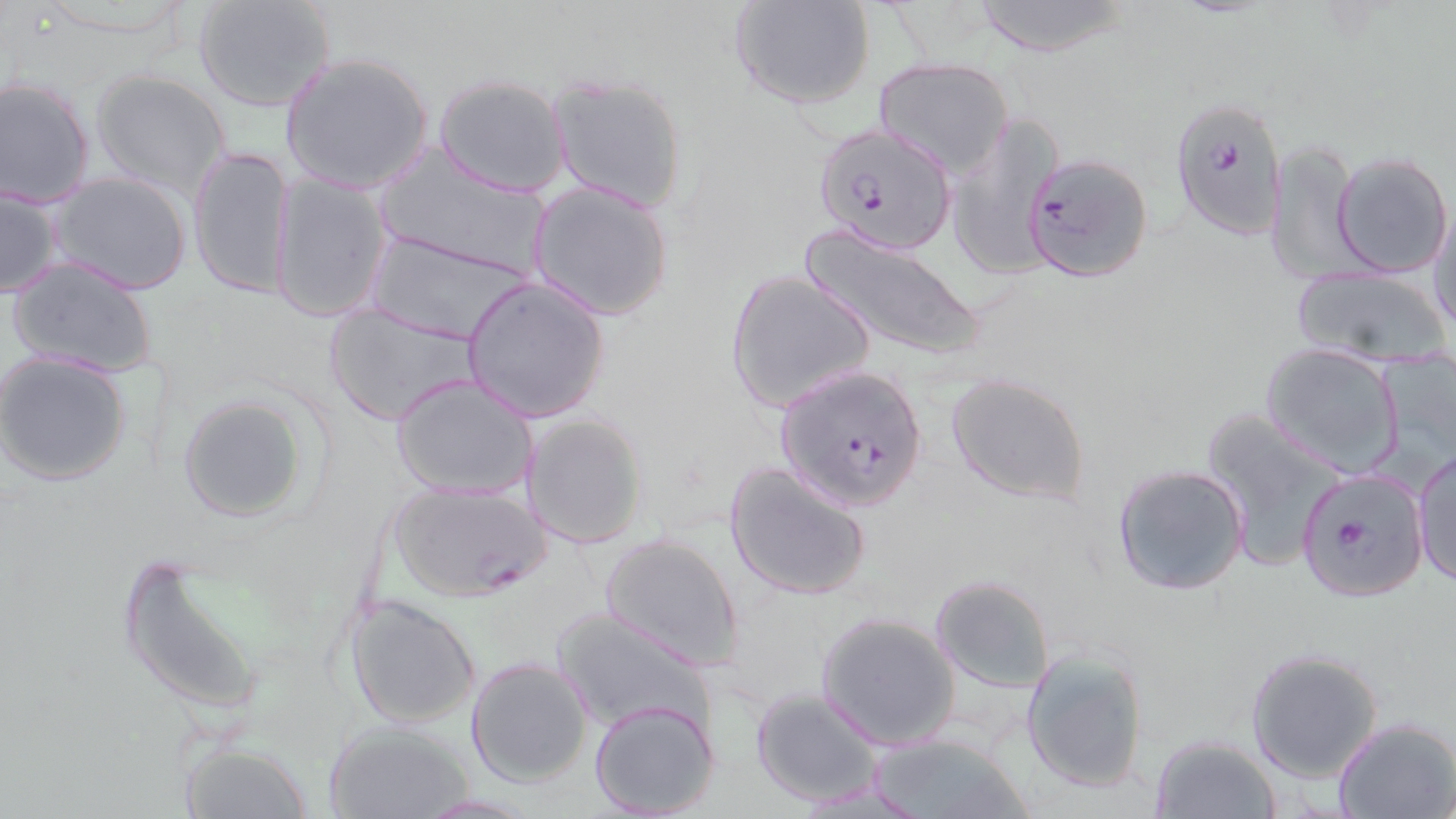
Plasmodium falciparum-infected red blood cell locations = approximate bounding boxes as (x1, y1, x2, y2) in pixels: (1171, 97, 1285, 240), (812, 122, 958, 255), (1022, 152, 1153, 282), (774, 363, 928, 513), (1297, 470, 1428, 601)
slide-level diagnosis = Plasmodium falciparum
preparation = thin blood film
uninfected red blood cell locations = approximate bounding boxes as (x1, y1, x2, y2) in pixels: (729, 0, 877, 110), (970, 0, 1133, 57), (192, 1, 338, 112), (237, 18, 397, 176), (279, 52, 434, 194), (871, 57, 1015, 180), (90, 70, 231, 198), (435, 74, 570, 198), (548, 74, 688, 212), (1, 77, 98, 209), (947, 113, 1065, 279), (1268, 137, 1365, 286), (189, 144, 295, 301), (1332, 152, 1452, 277), (374, 153, 553, 279), (49, 172, 193, 295), (269, 173, 393, 324), (528, 181, 674, 320), (0, 184, 65, 299), (1429, 197, 1456, 336), (801, 226, 984, 359), (367, 232, 533, 345), (7, 258, 157, 379), (1290, 264, 1450, 367), (724, 269, 877, 415), (461, 275, 610, 424), (324, 302, 481, 426), (1261, 341, 1405, 478), (1, 352, 132, 487), (945, 371, 1094, 505), (392, 373, 539, 501), (177, 394, 311, 522), (1204, 406, 1352, 567), (520, 412, 648, 550), (1412, 449, 1456, 586), (724, 460, 874, 602), (1112, 462, 1251, 597), (386, 480, 548, 603), (599, 533, 744, 670), (117, 553, 268, 720), (929, 574, 1057, 693), (343, 591, 482, 728), (553, 607, 715, 735), (816, 613, 961, 749), (1020, 647, 1150, 794), (1246, 648, 1384, 780), (465, 657, 593, 787), (751, 687, 887, 807), (590, 699, 720, 818), (1333, 718, 1456, 819), (322, 719, 478, 817), (865, 731, 1033, 819), (1149, 736, 1281, 817), (177, 740, 312, 818)
stain = May-Grünwald-Giemsa
field of view = single
magnification = 1000x
modality = optical microscopy
image size = 1456×819 pixels